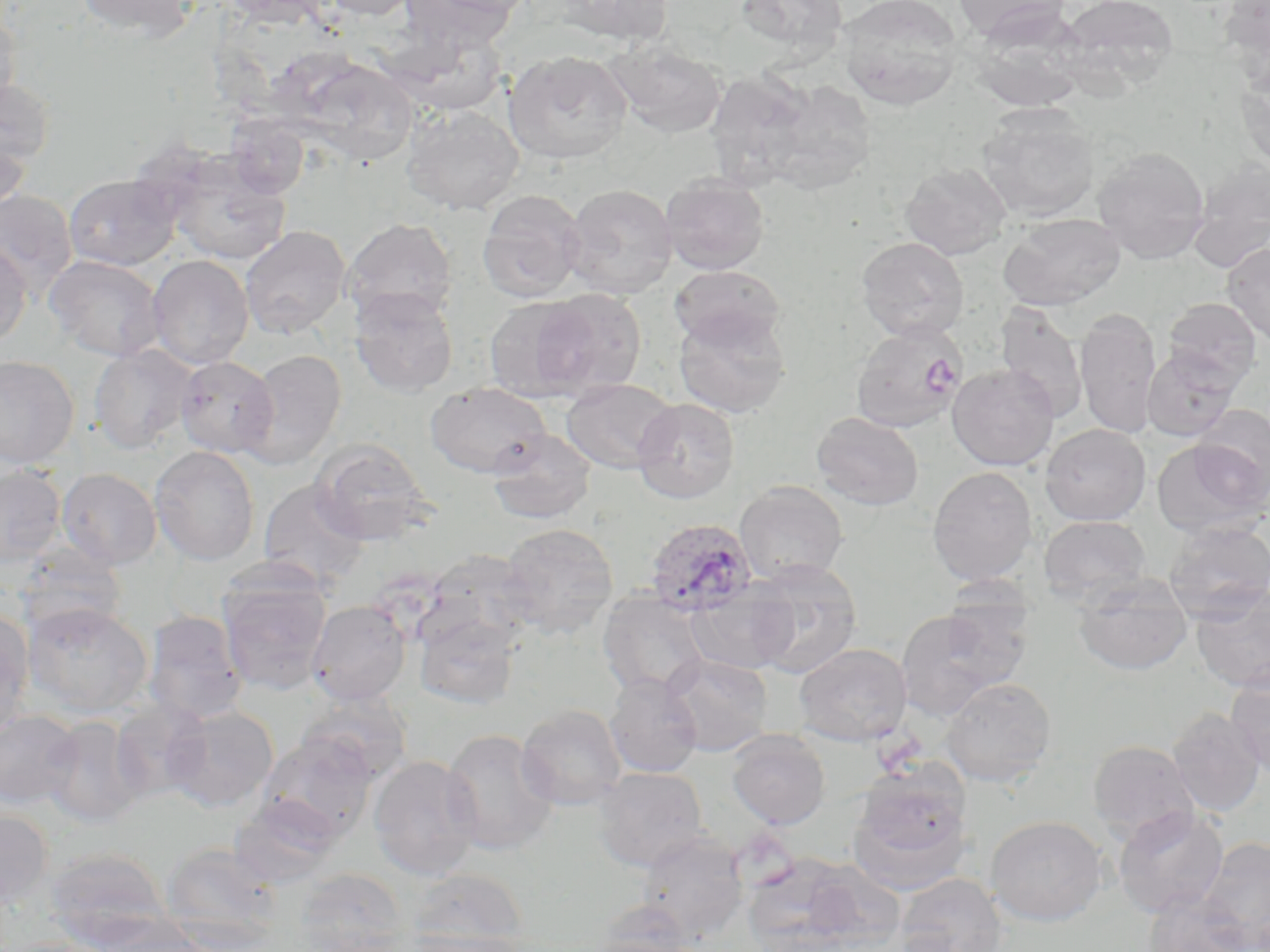
{
  "slide_level_diagnosis": "Plasmodium ovale",
  "platelet_locations": "approximate bounding boxes as (x1,y1)-(x2,y2) corner pairs in pixels: (923,356)-(961,393)",
  "modality": "light microscopy",
  "magnification": "1000x",
  "image_size": "1270×952 pixels",
  "stain": "May-Grünwald-Giemsa",
  "preparation": "thin blood film",
  "uninfected_red_blood_cell_locations": "approximate bounding boxes as (x1,y1)-(x2,y2) corner pairs in pixels: (73,0)-(199,40), (219,0)-(332,28), (319,0)-(421,20), (401,0)-(520,51), (561,0)-(674,45), (733,0)-(851,59), (836,0)-(964,110), (954,0)-(1072,44), (1056,0)-(1179,93), (1218,1)-(1270,77), (0,6)-(21,113), (971,7)-(1092,111), (382,27)-(510,117), (606,40)-(727,138), (504,50)-(632,165), (297,58)-(418,165), (1236,66)-(1270,174), (0,78)-(56,171), (401,105)-(524,215), (977,107)-(1100,223), (0,129)-(31,217), (1092,145)-(1211,263), (164,151)-(292,265), (1189,157)-(1270,269), (900,162)-(1012,260), (63,173)-(182,271), (661,174)-(769,274), (563,183)-(678,298), (0,189)-(78,297), (477,189)-(586,303), (998,213)-(1126,309), (342,218)-(457,325), (240,226)-(351,339), (856,237)-(969,341), (0,242)-(32,345), (1222,242)-(1270,348), (44,254)-(164,361), (147,255)-(254,369), (669,264)-(787,351), (349,285)-(458,398), (530,288)-(647,399), (483,295)-(596,401), (1162,297)-(1262,390), (994,302)-(1090,422), (1075,306)-(1162,439), (673,308)-(793,418), (850,321)-(966,433), (89,344)-(198,454), (1142,348)-(1239,441), (242,350)-(346,469), (0,355)-(80,469), (174,355)-(279,459), (946,364)-(1059,470), (561,378)-(678,473), (425,381)-(552,478), (631,397)-(740,504), (1191,405)-(1270,506), (811,411)-(924,511), (1041,424)-(1151,526), (488,429)-(597,525), (1152,437)-(1268,538), (311,438)-(435,546), (150,445)-(259,565), (0,466)-(66,566), (927,466)-(1038,586), (56,468)-(162,570), (258,480)-(370,588), (734,481)-(849,585), (1039,515)-(1152,606), (1162,520)-(1270,621), (498,522)-(619,639), (14,542)-(126,638), (420,550)-(539,655), (745,558)-(863,679), (1073,574)-(1193,676), (218,575)-(332,694), (685,582)-(798,676), (1190,584)-(1270,693), (597,591)-(712,699), (938,594)-(1035,689), (307,600)-(411,706), (22,602)-(152,718), (414,607)-(522,711), (895,608)-(1012,721), (0,609)-(34,739), (142,611)-(249,726), (794,643)-(912,746), (662,653)-(772,756), (1225,666)-(1270,778), (604,673)-(703,778), (940,677)-(1058,788), (295,691)-(414,786), (110,700)-(211,804), (516,704)-(627,811), (164,705)-(279,812), (1166,708)-(1266,817), (0,710)-(82,809), (41,716)-(144,828), (441,728)-(559,856), (727,729)-(830,830), (257,735)-(378,844), (1087,740)-(1198,843), (368,756)-(483,881), (593,767)-(708,871), (848,770)-(974,892), (229,795)-(341,889), (1112,806)-(1229,918), (0,809)-(54,910), (985,815)-(1107,926), (636,830)-(748,942), (1198,836)-(1270,951), (160,841)-(284,951), (44,847)-(173,949), (779,859)-(907,950), (293,867)-(411,952), (407,867)-(530,950), (893,872)-(1008,952), (1142,890)-(1256,952), (592,899)-(701,952), (80,914)-(208,952), (398,931)-(533,952), (580,934)-(700,952)",
  "plasmodium_ovale_infected_red_blood_cell_locations": "approximate bounding boxes as (x1,y1)-(x2,y2) corner pairs in pixels: (644,517)-(757,618)",
  "field_of_view": "single"
}